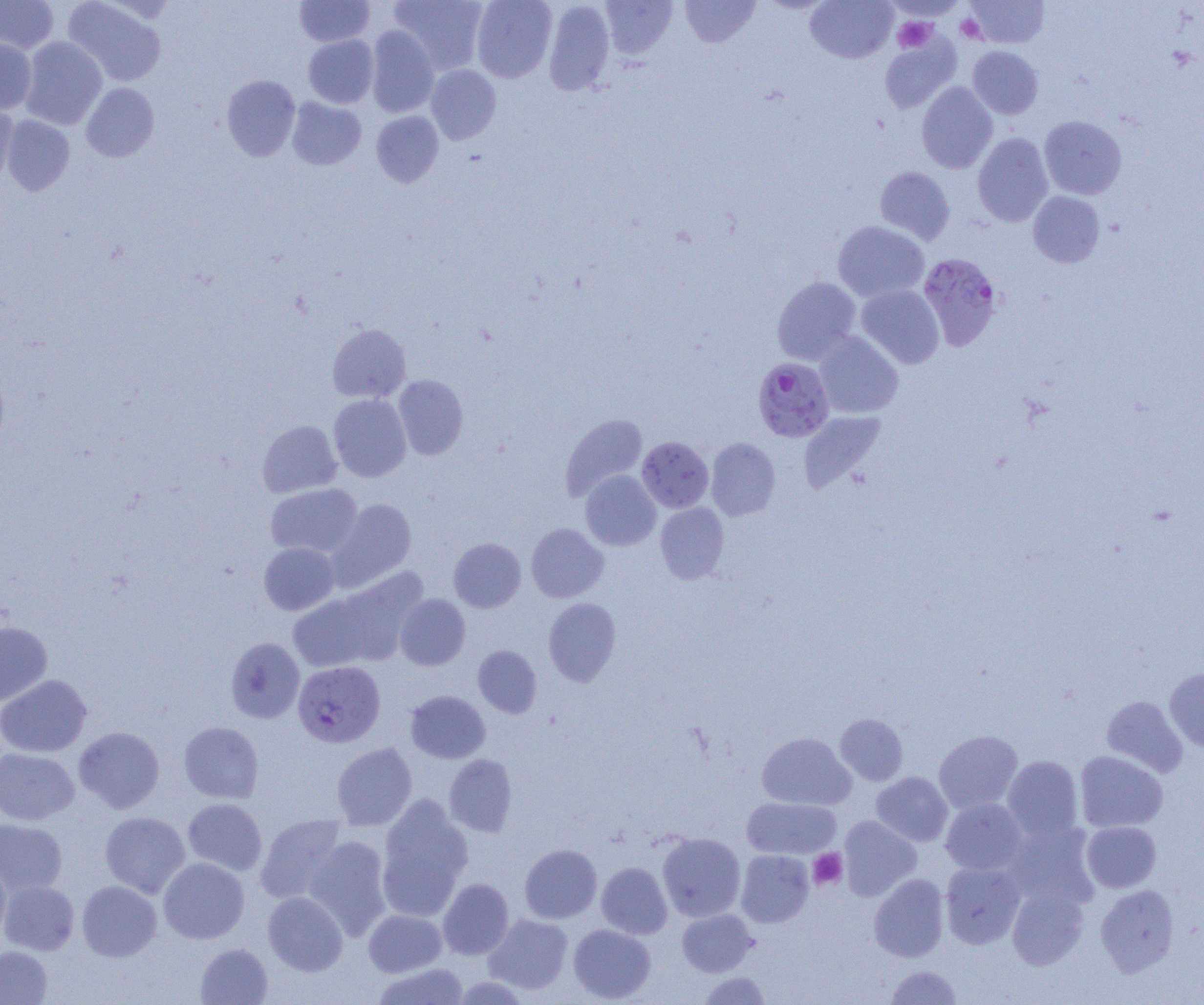

slide_level_diagnosis: Plasmodium falciparum
uninfected_red_blood_cell_locations: 'approximate bounding boxes as [x1, y1, x2, y2] in pixels: [0, 0, 59, 54], [63, 0, 167, 86], [295, 0, 375, 47], [388, 0, 488, 75], [471, 0, 557, 82], [543, 0, 615, 96], [681, 0, 760, 47], [805, 0, 898, 62], [966, 0, 1049, 48], [600, 1, 677, 59], [366, 26, 440, 117], [303, 35, 378, 108], [20, 36, 107, 130], [880, 37, 960, 112], [0, 38, 37, 115], [967, 46, 1042, 119], [426, 64, 501, 145], [221, 74, 300, 161], [81, 82, 159, 162], [916, 82, 997, 173], [287, 97, 366, 170], [0, 102, 19, 188], [371, 111, 443, 187], [1, 115, 75, 196], [1039, 115, 1126, 199], [973, 132, 1053, 227], [875, 166, 955, 245], [1028, 191, 1105, 267], [833, 221, 929, 302], [772, 276, 861, 365], [856, 284, 944, 369], [327, 324, 411, 402], [814, 331, 903, 419], [393, 374, 468, 460], [328, 394, 411, 482], [799, 411, 886, 493], [560, 413, 647, 501], [257, 420, 342, 498], [637, 436, 713, 513], [706, 438, 781, 521], [580, 470, 661, 551], [265, 483, 363, 558], [327, 498, 417, 591], [655, 502, 729, 584], [526, 523, 609, 602], [448, 538, 526, 612], [258, 542, 339, 615], [330, 569, 429, 666], [288, 593, 379, 672], [395, 594, 470, 671], [543, 598, 620, 686], [0, 621, 52, 706], [225, 637, 305, 723], [473, 645, 542, 718], [1165, 668, 1204, 752], [0, 674, 92, 757], [405, 690, 490, 764], [1101, 696, 1188, 777], [835, 713, 908, 785], [178, 721, 264, 804], [74, 726, 165, 813], [933, 730, 1023, 814], [757, 733, 855, 810], [332, 742, 417, 830], [0, 748, 79, 825], [1074, 750, 1168, 832], [444, 754, 517, 837], [1002, 755, 1084, 841], [871, 772, 953, 846], [377, 795, 474, 919], [742, 797, 841, 859], [941, 797, 1028, 875], [183, 798, 267, 875], [100, 812, 190, 898], [255, 813, 347, 904], [838, 815, 921, 901], [0, 818, 67, 896], [1001, 821, 1099, 911], [1081, 821, 1161, 892], [657, 832, 746, 922], [303, 836, 392, 940], [520, 844, 602, 923], [736, 850, 814, 927], [158, 857, 250, 944], [0, 859, 11, 944], [940, 861, 1025, 948], [596, 862, 672, 939], [869, 873, 950, 962], [438, 878, 514, 959], [0, 880, 79, 955], [77, 880, 161, 961], [1095, 884, 1179, 976], [1007, 885, 1089, 970], [263, 891, 348, 975], [363, 909, 447, 977], [677, 909, 758, 976], [484, 913, 573, 995], [568, 923, 655, 1003], [195, 943, 273, 1004], [0, 946, 52, 1004], [373, 962, 469, 1004], [886, 965, 961, 1004], [698, 971, 771, 1004]'
preparation: thin blood film
image_size: 1204×1005 pixels
magnification: 1000x
modality: optical microscopy
platelet_locations: 'approximate bounding boxes as [x1, y1, x2, y2] in pixels: [955, 14, 985, 42], [893, 17, 935, 52], [808, 849, 847, 889]'
field_of_view: single
plasmodium_falciparum_infected_red_blood_cell_locations: 'approximate bounding boxes as [x1, y1, x2, y2] in pixels: [919, 253, 1003, 351], [752, 357, 834, 441], [292, 660, 386, 747]'